State the blood parasite species.
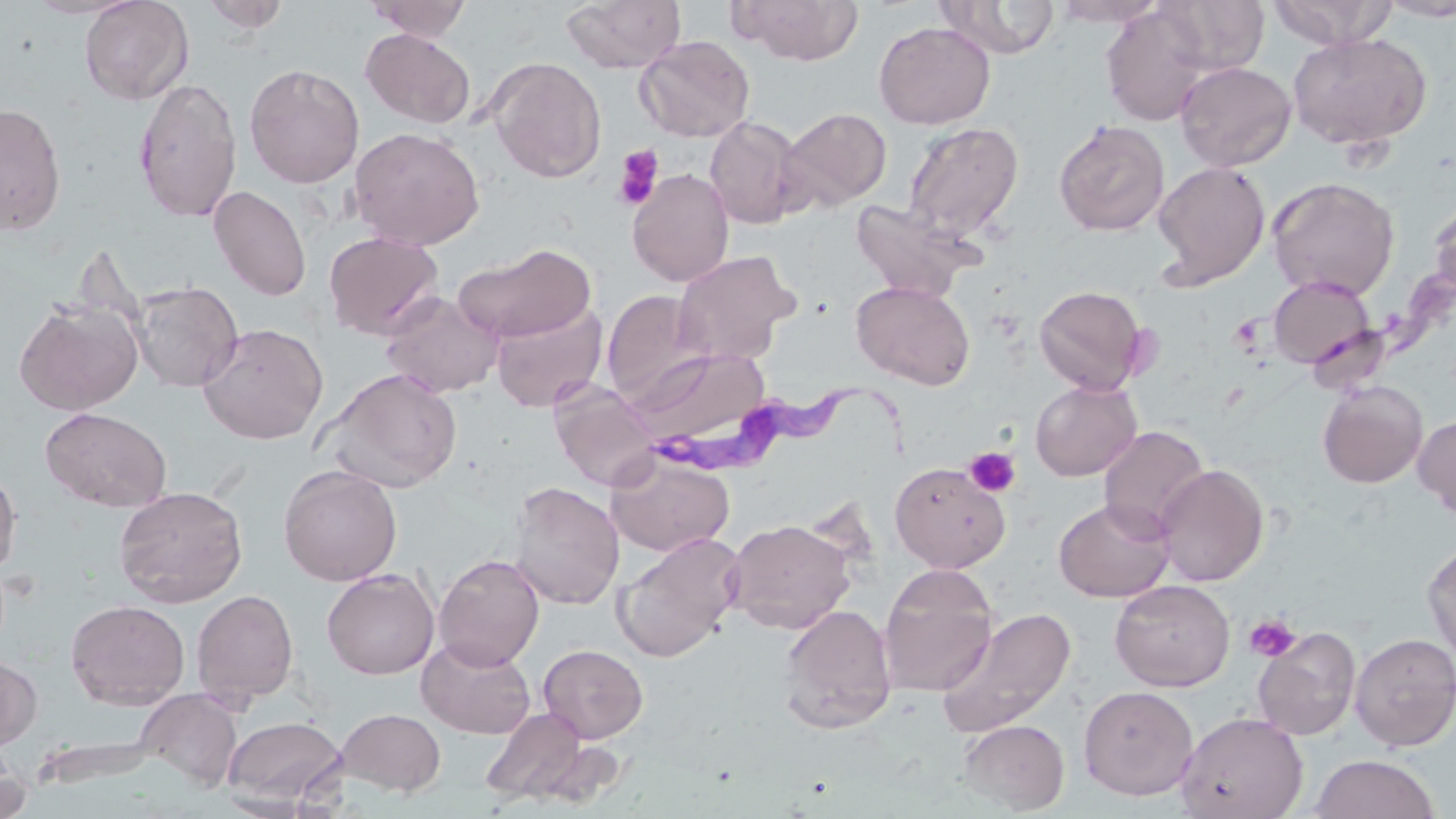

Trypanosoma brucei.

Summary:
  - Coordinate format: approximate bounding boxes as (x1,y1)-(x2,y2) corner pairs in pixels
  - Trypanosoma brucei locations: (668,375)-(917,483)
  - Platelet locations: (612,145)-(664,211), (964,447)-(1020,497), (1245,615)-(1301,662)
  - Uninfected red blood cell locations: (21,0)-(145,19), (79,0)-(195,105), (365,0)-(472,42), (561,0)-(686,73), (934,0)-(1061,59), (1052,0)-(1167,27), (1155,0)-(1270,75), (1269,0)-(1398,48), (1377,0)-(1456,21), (201,1)-(290,34), (732,1)-(865,65), (1099,5)-(1214,125), (873,21)-(995,129), (361,28)-(475,129), (1287,31)-(1432,150), (634,35)-(755,143), (486,57)-(607,183), (1175,60)-(1296,172), (244,63)-(364,188), (133,76)-(242,223), (0,102)-(66,236), (779,107)-(892,212), (705,116)-(806,230), (1053,118)-(1170,236), (903,121)-(1024,240), (349,126)-(485,250), (1151,160)-(1271,290), (626,168)-(734,287), (1267,177)-(1400,301), (209,186)-(312,301), (1428,197)-(1456,305), (849,198)-(979,302), (323,231)-(445,341), (453,242)-(596,343), (672,250)-(799,365), (1268,276)-(1375,369), (851,279)-(975,390), (131,280)-(243,393), (1033,285)-(1149,395), (380,291)-(504,398), (602,291)-(708,405), (14,298)-(143,415), (490,302)-(608,413), (197,322)-(328,444), (630,346)-(768,442), (320,367)-(463,493), (1030,379)-(1142,481), (548,380)-(661,491), (1318,381)-(1428,488), (40,406)-(172,512), (1414,414)-(1456,518), (1098,425)-(1209,538), (606,453)-(735,557), (890,461)-(1010,573), (278,463)-(402,586), (1155,463)-(1268,587), (0,467)-(21,577), (507,481)-(624,610), (113,485)-(248,607), (1053,497)-(1175,602), (725,518)-(857,634), (612,532)-(744,663), (1423,540)-(1456,668), (434,553)-(545,670), (877,565)-(998,696), (321,568)-(440,679), (1110,580)-(1235,692), (191,589)-(299,705), (65,599)-(190,710), (776,604)-(897,735), (936,606)-(1077,737), (1253,626)-(1361,740), (1350,632)-(1456,751), (417,637)-(536,738), (538,644)-(648,743), (0,654)-(42,751), (1078,685)-(1199,800), (137,689)-(244,794), (479,706)-(590,807), (336,708)-(446,796), (1175,710)-(1308,819), (223,716)-(346,806), (958,718)-(1069,814), (0,745)-(29,819), (1310,754)-(1441,819)
  - Field of view: single
  - Stain: May-Grünwald-Giemsa
  - Image size: 1456×819 pixels
  - Preparation: thin blood film
  - Modality: optical microscopy
  - Magnification: 1000x